Name the parasite shown.
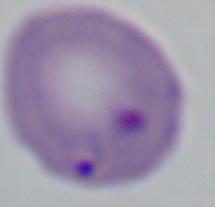
This is Babesia.

Summary:
  - Magnification: 1000x
  - Modality: photomicrograph